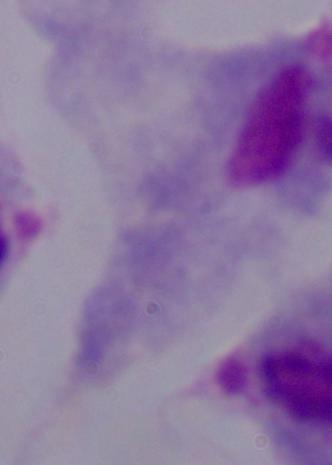

{
  "modality": "micrograph",
  "magnification": "1000x",
  "identification": "trichomonad"
}